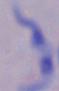 Photomicrograph. A trypanosome is seen. 1000x magnification.